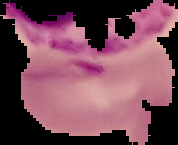
Result: malaria parasites identified. The area outside the segmented cell region is set to black. From a thin blood film. Image is 178×145 pixels.